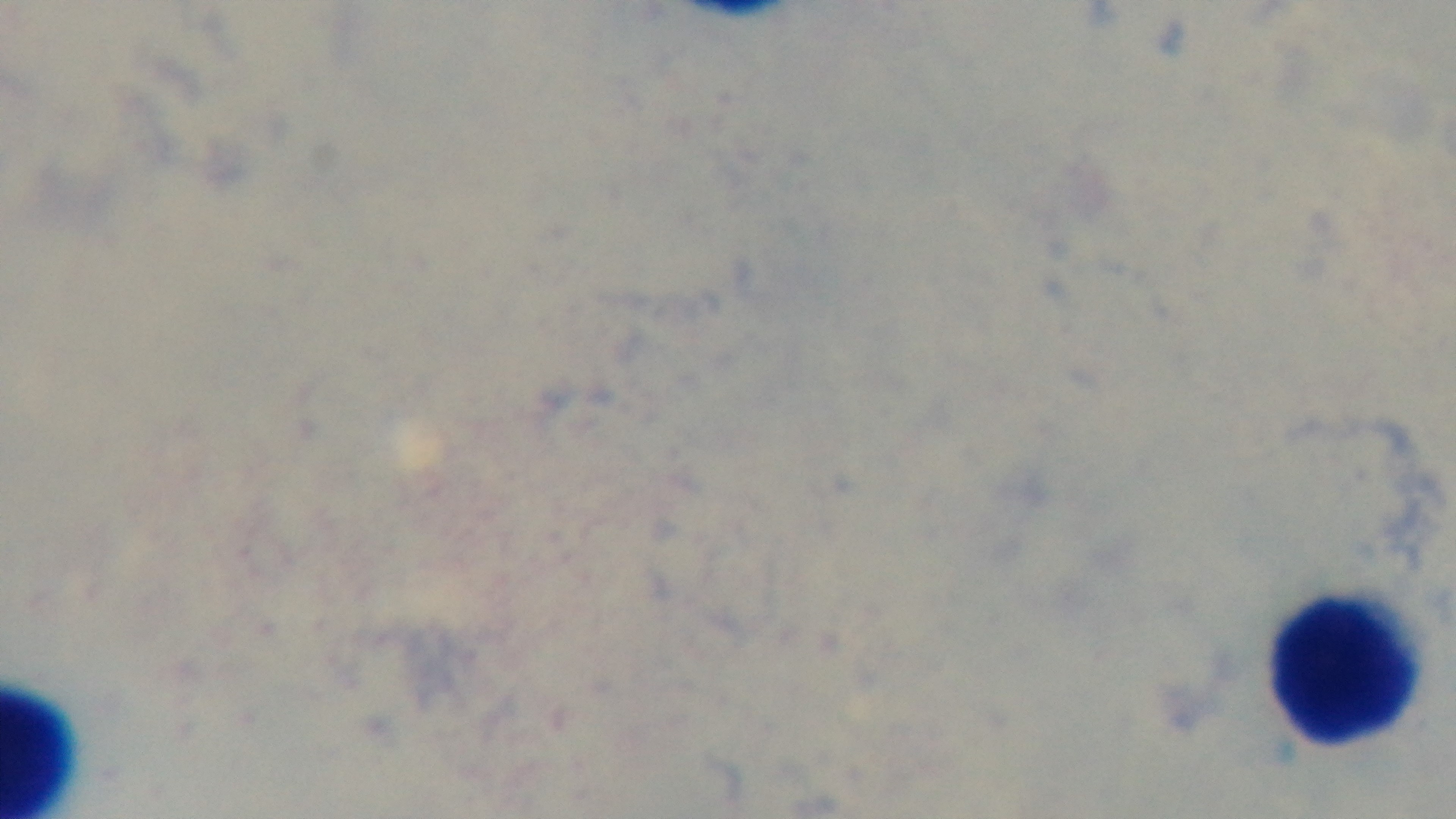 Giemsa-stained. Preparation: thick smear. 100x oil-immersion objective. Single field of view. Captured with a mounted 4K digital camera. Malaria status: negative. Photomicrograph.